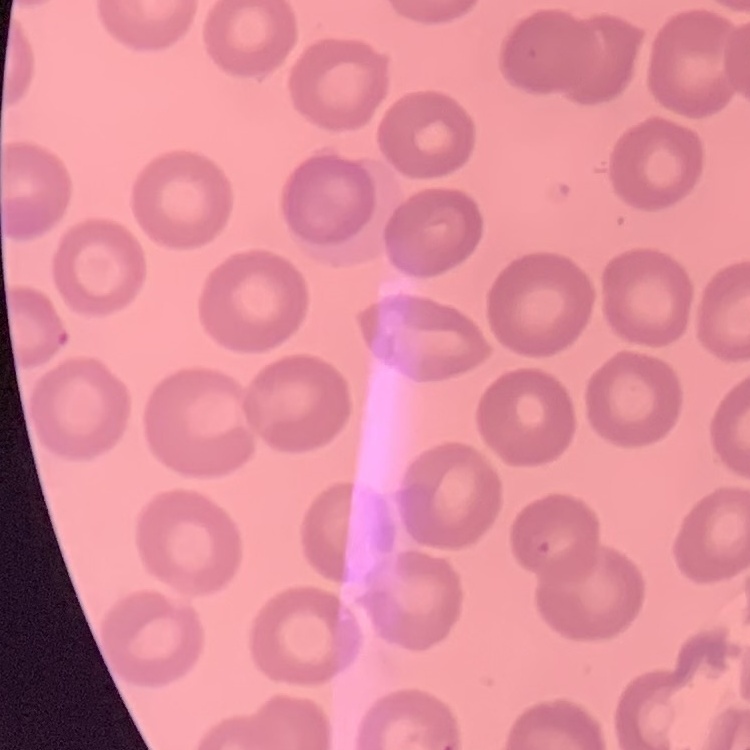

The erythrocytes show no rouleaux formation. Thin blood smear. One tile cut from a larger photomicrograph. Stained with either Field's or Giemsa.